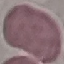
Summary:
  - Result: no malaria parasites detected
  - Image type: cell patch, automatically extracted from a larger field of view and resized to 64 × 64 pixels
  - Preparation: thin blood smear
  - Stain: Giemsa
  - Capture: smartphone camera at the microscope eyepiece